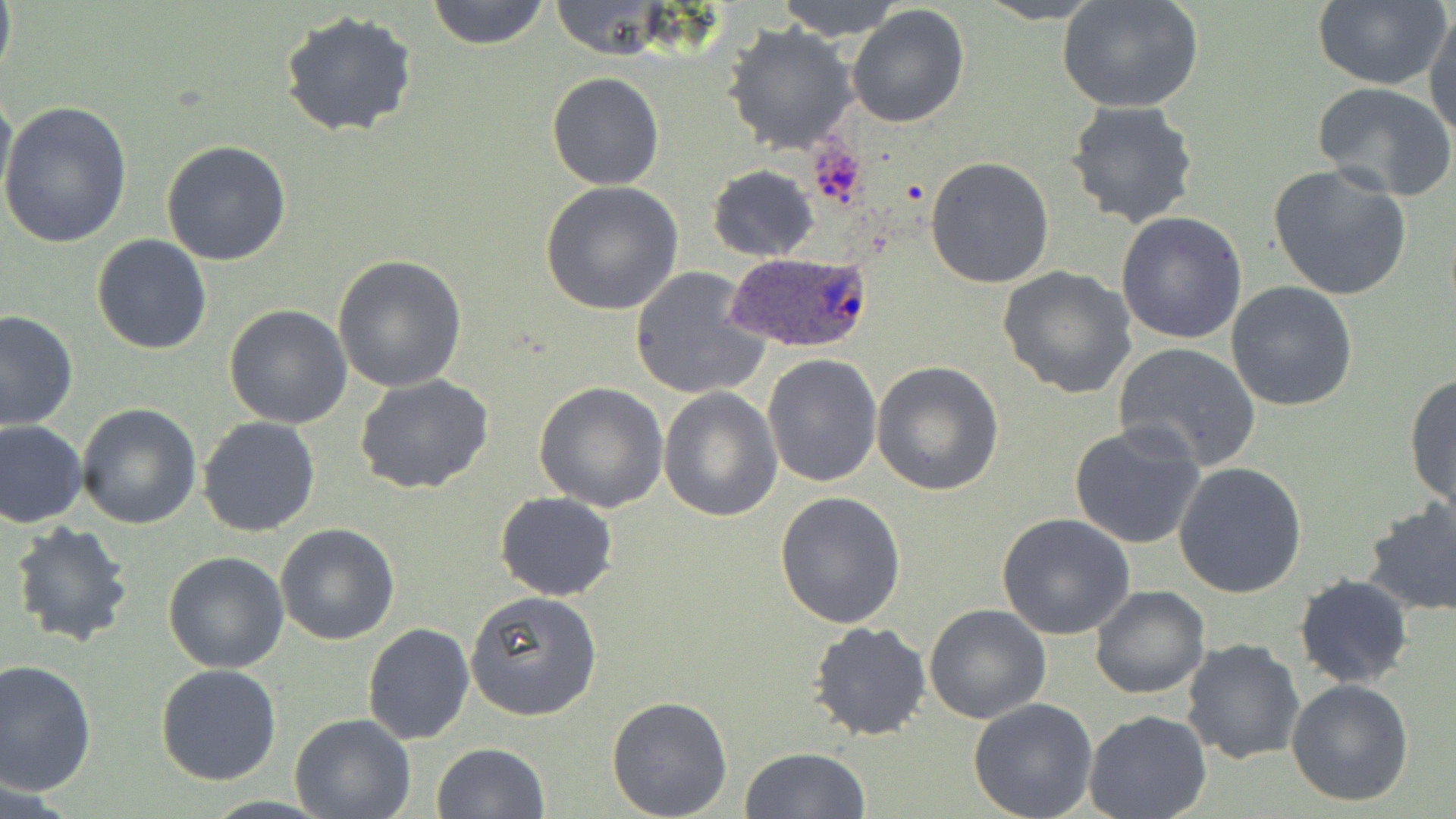

slide-level diagnosis = Plasmodium ovale
field of view = one of a larger specimen
modality = light microscopy
stain = May-Grünwald-Giemsa
preparation = thin blood smear
Plasmodium ovale-infected red blood cell locations = approximate bounding boxes as (x1, y1, x2, y2) in pixels: (727, 251, 875, 354)
uninfected red blood cell locations = approximate bounding boxes as (x1, y1, x2, y2) in pixels: (0, 0, 17, 90), (426, 0, 550, 49), (548, 0, 671, 58), (774, 0, 910, 40), (973, 0, 1106, 24), (1055, 0, 1204, 114), (1311, 0, 1449, 89), (846, 3, 970, 128), (1424, 10, 1456, 139), (280, 11, 419, 138), (724, 23, 856, 155), (546, 73, 665, 190), (1312, 81, 1455, 201), (0, 83, 16, 209), (1064, 100, 1203, 230), (0, 101, 132, 252), (160, 140, 292, 266), (924, 156, 1055, 288), (1265, 163, 1412, 303), (706, 164, 820, 262), (540, 182, 684, 318), (1116, 209, 1248, 344), (92, 234, 212, 354), (333, 254, 468, 393), (628, 265, 769, 401), (997, 265, 1138, 398), (1226, 281, 1359, 411), (223, 305, 352, 429), (0, 309, 78, 431), (1112, 342, 1263, 470), (762, 353, 884, 488), (872, 361, 1004, 498), (659, 368, 879, 500), (1403, 369, 1456, 512), (354, 376, 496, 495), (533, 382, 668, 512), (659, 388, 784, 522), (77, 403, 202, 529), (197, 416, 322, 538), (0, 420, 87, 528), (1067, 420, 1208, 552), (1174, 461, 1308, 597), (495, 491, 618, 601), (773, 491, 907, 630), (1360, 500, 1456, 620), (996, 515, 1136, 641), (8, 520, 134, 649), (275, 523, 399, 645), (163, 552, 289, 673), (1295, 574, 1414, 689), (1089, 585, 1210, 699), (465, 590, 603, 721), (923, 603, 1052, 724), (806, 620, 932, 742), (362, 622, 475, 746), (1181, 638, 1306, 765), (0, 658, 99, 796), (155, 664, 284, 786), (1286, 678, 1415, 807), (606, 696, 733, 818), (969, 699, 1098, 818), (1084, 711, 1213, 819), (289, 713, 415, 819), (431, 742, 548, 819), (739, 747, 870, 819)
magnification = 1000x
image size = 1456×819 pixels
platelet locations = approximate bounding boxes as (x1, y1, x2, y2) in pixels: (807, 141, 869, 209)